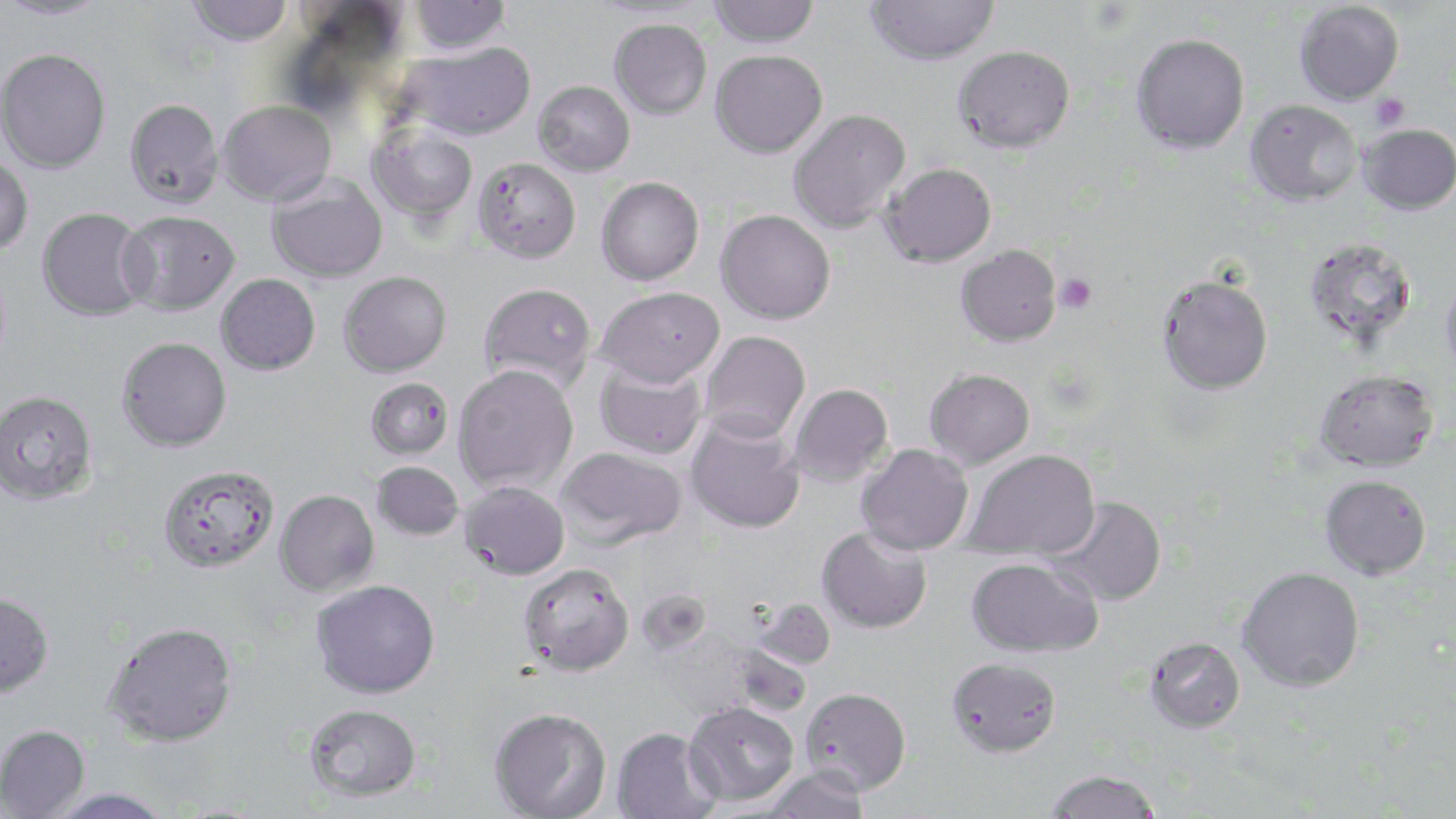

Approximate bounding boxes as (x1,y1)-(x2,y2) corner pairs in pixels. Platelet locations: (1369,94)-(1410,130), (1055,273)-(1097,313). Uninfected red blood cell locations: (0,0)-(111,21), (185,0)-(293,47), (409,0)-(510,55), (708,0)-(820,48), (864,0)-(1000,66), (589,1)-(715,21), (1294,2)-(1404,108), (609,19)-(712,119), (1130,33)-(1249,155), (402,42)-(536,141), (952,45)-(1075,154), (1,48)-(111,174), (710,50)-(828,158), (533,80)-(635,177), (124,98)-(224,209), (217,100)-(336,206), (1246,100)-(1361,208), (787,109)-(910,233), (366,123)-(478,223), (1357,125)-(1456,217), (0,155)-(33,255), (472,157)-(581,263), (881,162)-(997,267), (266,173)-(388,284), (595,176)-(704,285), (36,207)-(151,321), (715,209)-(836,324), (117,210)-(240,315), (1304,239)-(1418,349), (955,245)-(1061,347), (338,271)-(451,377), (216,274)-(320,375), (1155,274)-(1274,396), (1440,275)-(1456,382), (477,282)-(596,392), (595,286)-(724,388), (699,331)-(810,444), (116,337)-(232,452), (595,360)-(707,459), (452,364)-(578,493), (924,368)-(1035,469), (1315,371)-(1438,473), (364,378)-(453,461), (787,383)-(893,487), (0,389)-(98,505), (684,415)-(806,534), (855,443)-(974,555), (556,446)-(687,549), (963,449)-(1100,561), (371,461)-(464,541), (157,464)-(279,574), (1319,475)-(1431,580), (459,481)-(569,580), (275,489)-(380,595), (1048,496)-(1167,607), (816,525)-(932,634), (965,556)-(1102,658), (517,563)-(634,676), (1237,565)-(1364,692), (311,579)-(440,699), (636,587)-(712,657), (0,590)-(54,697), (751,597)-(836,670), (104,620)-(238,747), (1145,637)-(1246,733), (731,643)-(812,718), (946,656)-(1061,758), (800,687)-(911,795), (683,701)-(799,807), (304,703)-(422,801), (489,706)-(611,819), (0,725)-(90,818), (612,726)-(722,819), (761,768)-(868,818), (1042,769)-(1163,819), (45,787)-(174,819). Slide-level diagnosis: Plasmodium falciparum. Thin blood film. One field of a larger specimen. Image is 1456×819 pixels. May-Grünwald-Giemsa stain. 1000x magnification. Optical microscopy.